Name the parasite shown.
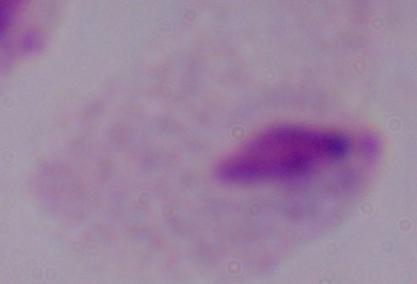
A trichomonad.

1000x magnification. Micrograph.